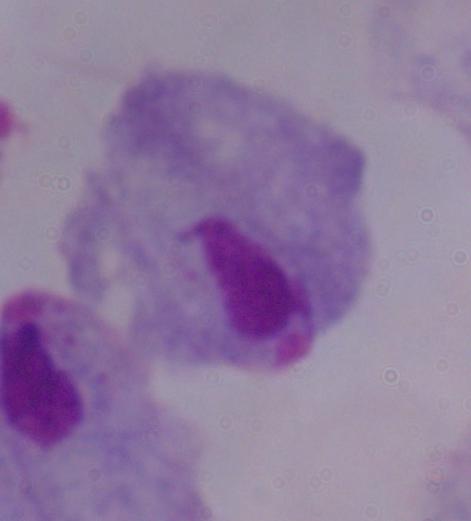

Summary:
  - Identification: trichomonad
  - Modality: photomicrograph
  - Magnification: 1000x